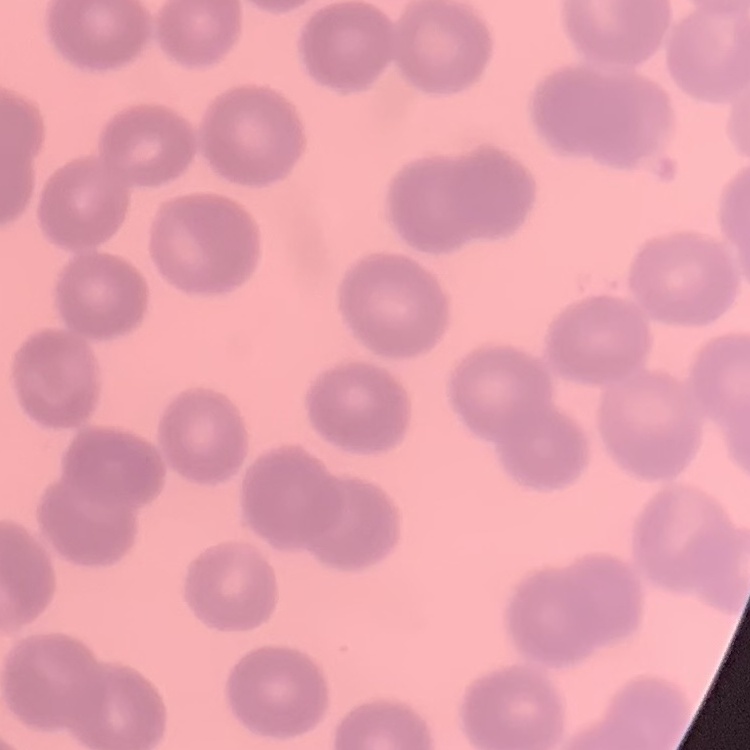 The red blood cells show no rouleaux formation. Stained with either Field's or Giemsa. One tile cut from a larger photomicrograph. Thin peripheral smear.